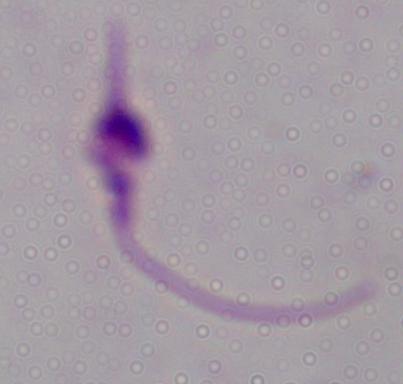
1000x magnification. Photomicrograph. A Leishmania parasite is shown.